Locate and identify every blood parasite.
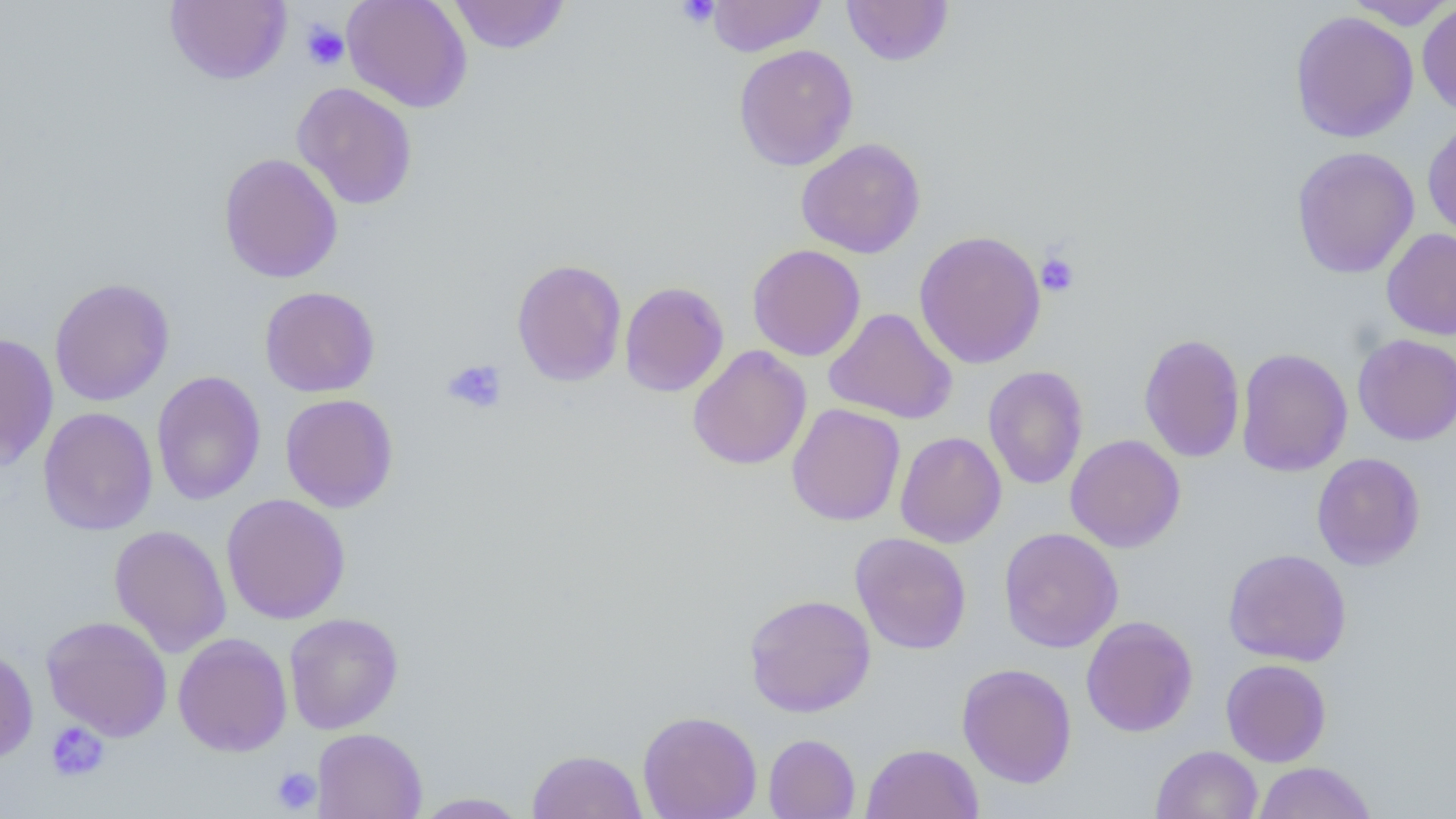
No blood parasites seen.

Summary:
  - Coordinate format: approximate bounding boxes as (x1, y1, x2, y2) in pixels
  - Uninfected red blood cell locations: (165, 0, 291, 85), (342, 0, 472, 113), (448, 0, 570, 54), (706, 0, 826, 57), (841, 0, 953, 66), (1345, 0, 1456, 30), (1417, 1, 1456, 118), (1290, 10, 1419, 143), (733, 44, 858, 171), (292, 82, 418, 209), (1422, 119, 1456, 242), (795, 138, 926, 259), (1291, 146, 1420, 279), (218, 152, 343, 283), (1381, 227, 1456, 340), (914, 230, 1046, 368), (747, 244, 865, 362), (512, 258, 627, 387), (49, 277, 175, 406), (619, 281, 729, 397), (259, 286, 380, 398), (823, 307, 957, 425), (0, 332, 59, 470), (1138, 333, 1246, 463), (1353, 333, 1456, 445), (687, 345, 811, 470), (1235, 347, 1353, 477), (983, 365, 1089, 490), (151, 371, 266, 505), (280, 393, 399, 513), (786, 403, 905, 526), (38, 407, 158, 536), (895, 431, 1006, 548), (1065, 434, 1185, 552), (1311, 452, 1425, 570), (221, 493, 351, 624), (109, 524, 232, 658), (998, 527, 1123, 653), (850, 532, 972, 655), (1223, 549, 1351, 667), (743, 593, 876, 717), (284, 612, 404, 734), (41, 615, 173, 742), (1081, 615, 1198, 737), (172, 633, 292, 757), (0, 645, 38, 763), (1220, 658, 1331, 767), (957, 662, 1077, 788), (638, 710, 762, 818), (312, 727, 428, 819), (763, 733, 860, 818), (861, 742, 983, 819), (1150, 745, 1263, 819), (527, 749, 648, 819), (1252, 761, 1377, 819), (412, 792, 530, 818)
  - Platelet locations: (675, 0, 720, 28), (300, 21, 349, 70), (1036, 251, 1080, 297), (443, 360, 508, 414), (44, 722, 110, 782), (271, 767, 321, 814)
  - Slide-level diagnosis: negative for blood parasites
  - Field of view: single
  - Magnification: 1000x
  - Preparation: thin blood film
  - Modality: optical microscopy
  - Image size: 1456×819 pixels